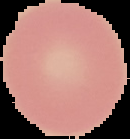

preparation = thin blood smear
image type = cell region segmented out of the field of view; surrounding area masked to black
malaria status = uninfected
image size = 130×139 pixels